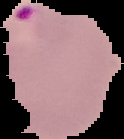
image size = 124×139 pixels
preparation = thin blood smear
malaria status = parasitized
image type = cell region segmented out of the field of view; surrounding area masked to black